State the blood parasite species.
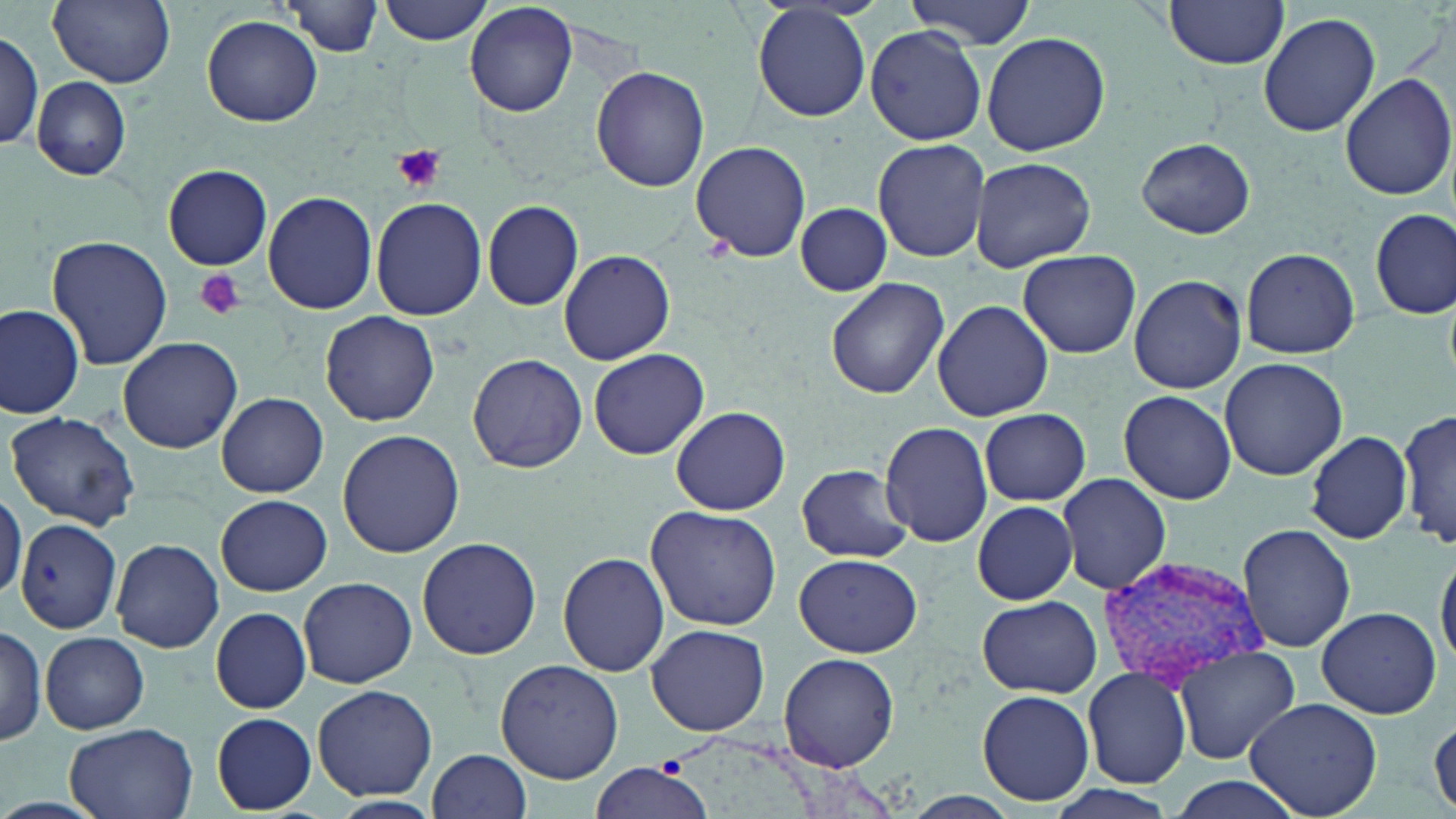

Plasmodium vivax.

Approximate bounding boxes as (x1,y1)-(x2,y2) corner pairs in pixels. Plasmodium vivax-infected red blood cell locations: (1096,554)-(1264,691). Platelet locations: (394,145)-(447,190), (196,270)-(246,322). Uninfected red blood cell locations: (48,0)-(175,88), (376,0)-(495,45), (906,0)-(1035,48), (1163,0)-(1291,69), (42,1)-(151,173), (286,1)-(382,55), (465,2)-(577,116), (752,4)-(871,122), (1258,12)-(1381,137), (202,15)-(323,127), (864,26)-(987,145), (0,29)-(44,154), (982,30)-(1111,157), (592,66)-(709,191), (1339,72)-(1455,202), (30,76)-(132,179), (872,137)-(992,263), (1135,138)-(1257,238), (691,140)-(812,262), (968,156)-(1098,274), (163,164)-(273,271), (262,190)-(378,315), (370,197)-(486,320), (482,200)-(584,310), (794,202)-(892,297), (1372,207)-(1454,319), (44,235)-(173,371), (1240,247)-(1360,358), (559,250)-(676,364), (1017,251)-(1140,358), (1128,274)-(1247,393), (827,278)-(949,398), (932,299)-(1054,423), (0,303)-(86,419), (320,311)-(440,425), (117,336)-(244,454), (589,348)-(709,460), (469,355)-(587,472), (1218,357)-(1348,480), (1118,390)-(1236,504), (217,393)-(329,497), (670,404)-(791,516), (979,407)-(1090,505), (1400,407)-(1455,551), (5,409)-(143,532), (880,422)-(992,546), (337,429)-(465,558), (1303,429)-(1414,545), (796,464)-(913,562), (1057,472)-(1172,596), (0,484)-(25,607), (215,494)-(331,595), (972,500)-(1078,604), (645,504)-(781,632), (17,518)-(121,633), (1236,522)-(1356,652), (416,536)-(541,660), (111,538)-(224,653), (1436,549)-(1456,671), (558,552)-(669,677), (795,552)-(922,657), (298,576)-(416,688), (978,596)-(1100,698), (211,606)-(313,712), (1316,606)-(1444,719), (646,623)-(770,737), (0,624)-(48,745), (41,632)-(149,733), (1172,645)-(1299,765), (779,652)-(900,774), (494,660)-(624,785), (1081,666)-(1192,789), (313,683)-(439,802), (976,689)-(1095,806), (1244,697)-(1384,819), (211,712)-(317,813), (1430,713)-(1456,816), (64,722)-(199,819), (428,748)-(531,819), (588,759)-(711,819), (1162,777)-(1307,819), (1039,781)-(1181,819), (901,792)-(1023,819). May-Grünwald-Giemsa-stained preparation. Light microscopy. Thin blood smear. Captured at 1000x magnification. Image is 1456×819 pixels. One field of a larger specimen.